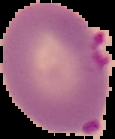
Summary:
  - Image size: 115×139 pixels
  - Preparation: thin blood smear
  - Result: Plasmodium parasites identified
  - Image type: segmented cell region on a black background